Describe the morphology of the red blood cells.
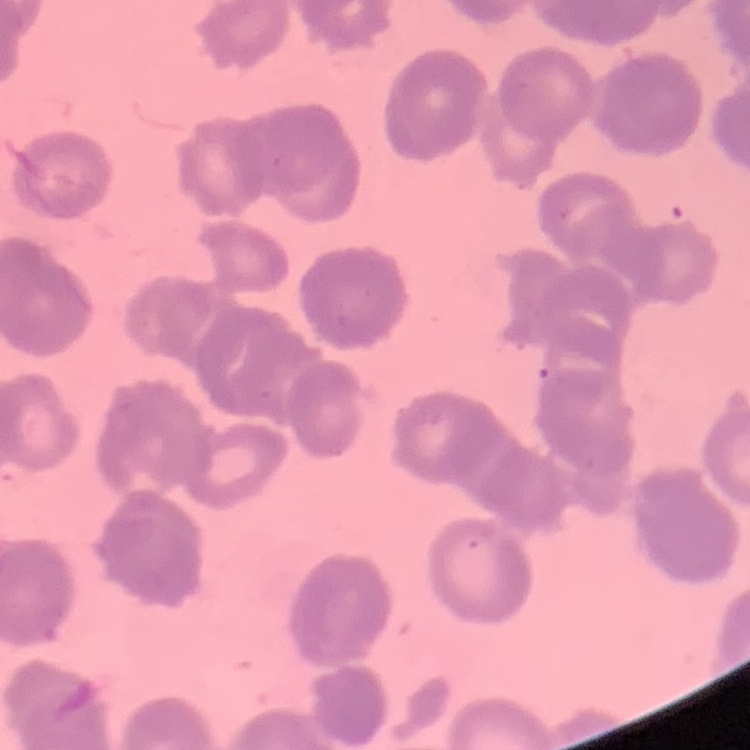
Rouleaux formation.

Square crop of a larger photomicrograph. Thin blood smear. Field's or Giemsa stain.